Identify the cell.
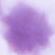
This is an erythrocyte.

magnification = 1000x
modality = micrograph